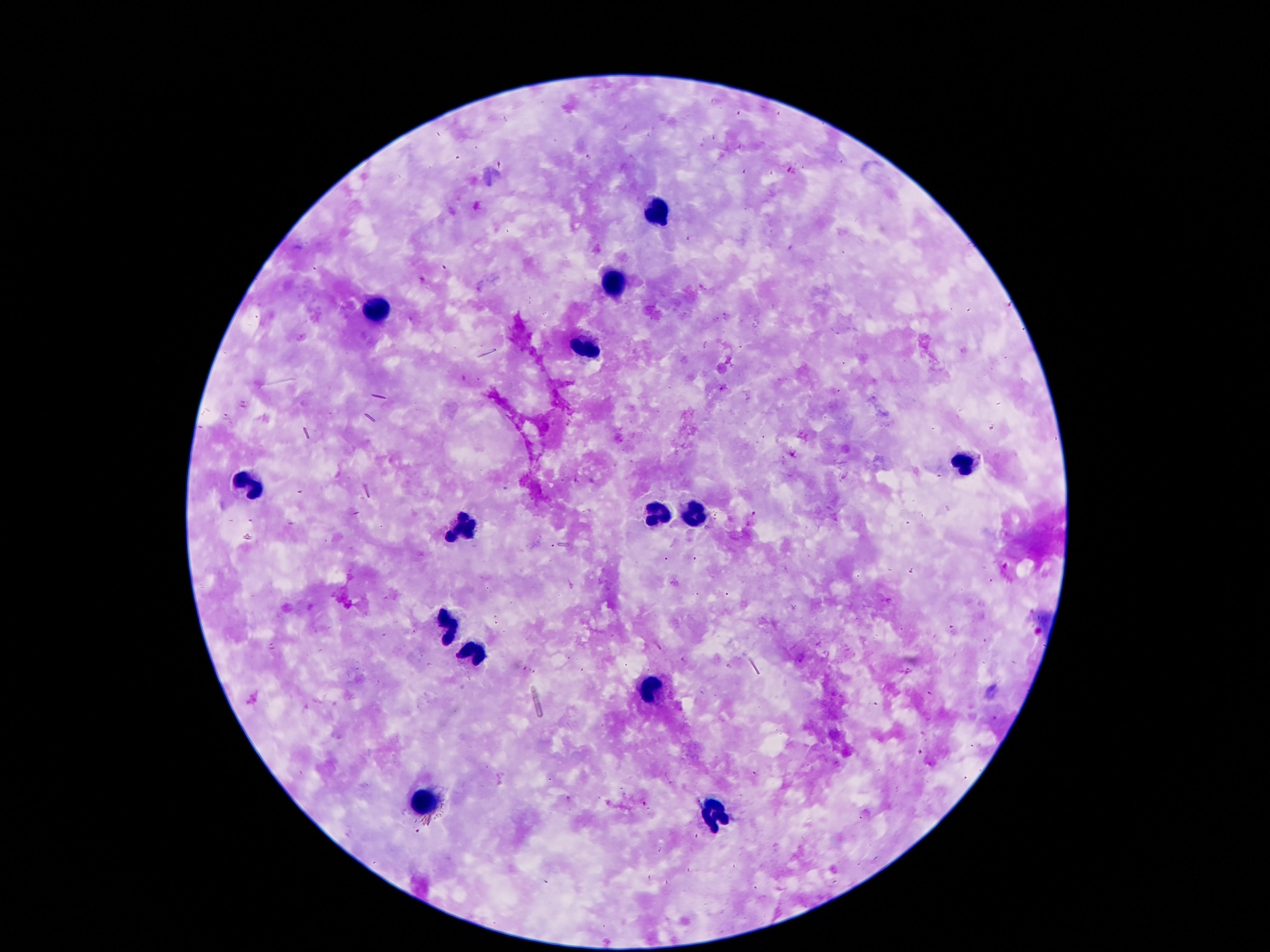

Approximate centers as (x, y) in pixels.
Summary:
  - Leukocyte locations: (658, 213), (617, 285), (381, 305), (585, 350), (964, 461), (248, 486), (660, 513), (695, 515), (465, 528), (450, 627), (474, 650), (651, 689), (425, 803), (715, 813)
  - Capture: smartphone camera through the microscope eyepiece
  - Image size: 1270×952 pixels
  - Patient malaria status: negative
  - Magnification: 100x
  - Preparation: thick peripheral-blood smear
  - Stain: Giemsa
  - Field of view: one from this slide